Describe the morphology of the erythrocytes.
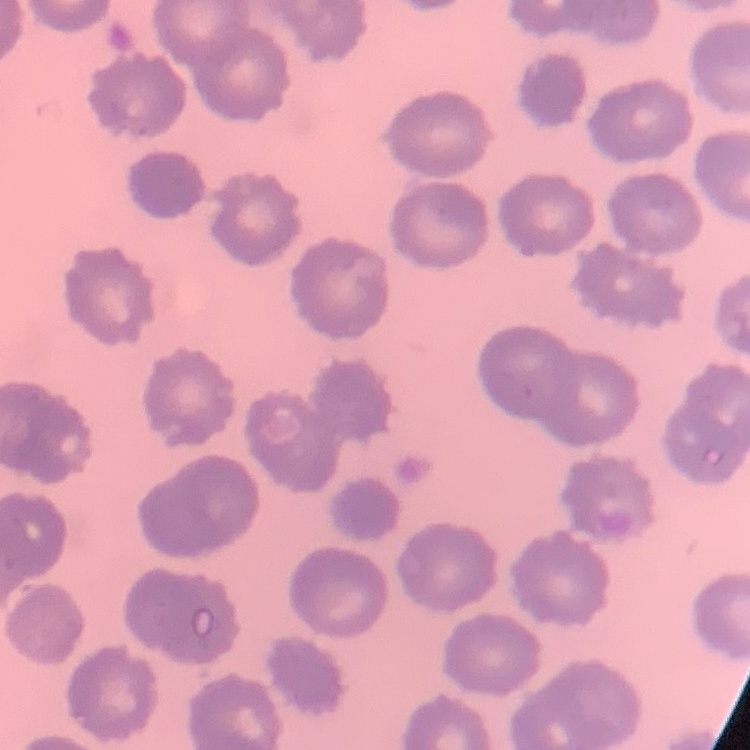

No rouleaux formation.

Summary:
  - Image type: one tile cut from a larger photomicrograph
  - Stain: Field's or Giemsa
  - Preparation: thin blood film